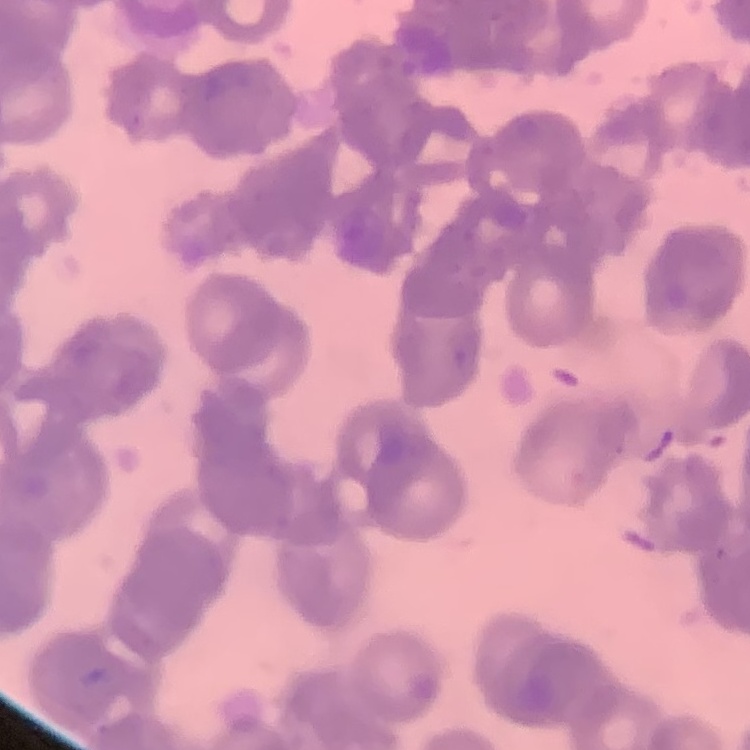

erythrocyte morphology = rouleaux formation
stain = Field's or Giemsa
preparation = thin blood film
image type = one tile cut from a larger photomicrograph